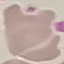

result = negative for malaria parasites
stain = Giemsa
preparation = thin blood smear
capture = smartphone through the microscope eyepiece
image type = cell patch, automatically extracted from a larger field of view and resized to 64 × 64 pixels